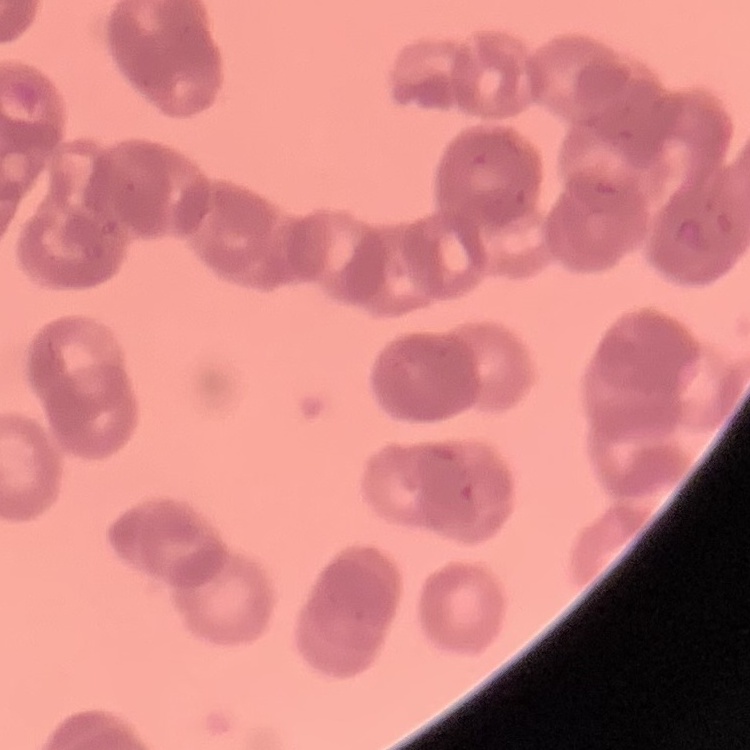

Summary:
  - Red blood cell morphology: rouleaux formation
  - Image type: square crop of a larger photomicrograph
  - Stain: Field's or Giemsa
  - Preparation: thin blood film